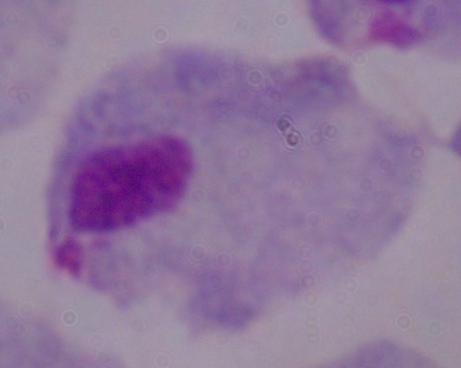

magnification: 1000x
modality: micrograph
identification: trichomonad